Assess this cell for malaria.
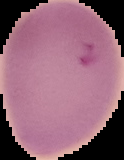

Parasitized.

Summary:
  - Image type: segmented cell region with the area outside set to black
  - Preparation: thin blood smear
  - Image size: 124×160 pixels